Report the malaria status of this cell.
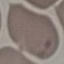
It is uninfected.

stain = Giemsa
preparation = thin smear
image type = automatically extracted cell patch, resized to 64 × 64 pixels
capture = smartphone through the microscope eyepiece